Classify this cell by malaria status.
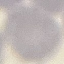
It is uninfected.

Thin blood smear. Giemsa-stained preparation. Automatically extracted cell patch, resized to 64 × 64 pixels. Acquired by smartphone through the microscope eyepiece.